Comment on the morphology of the erythrocytes.
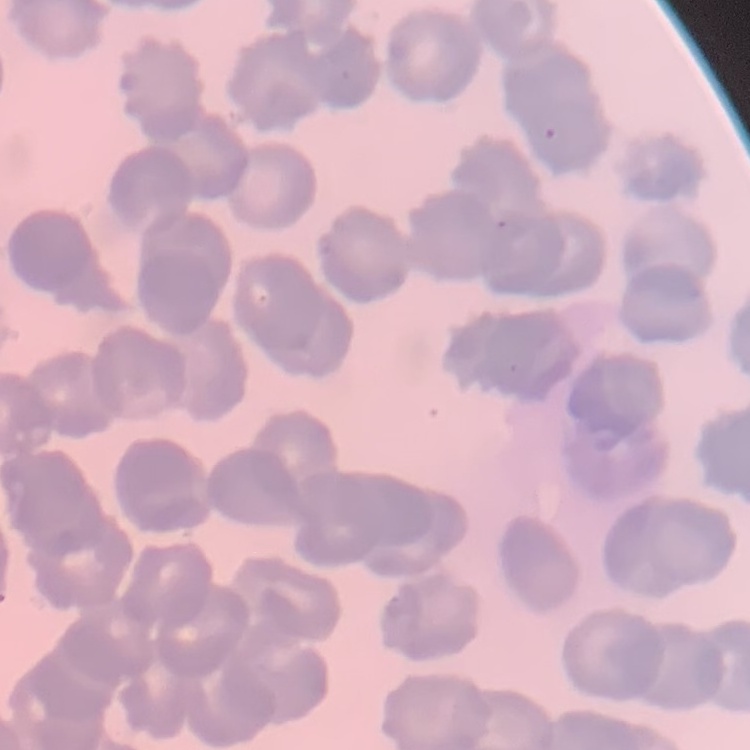
Rouleaux formation.

Summary:
  - Stain: Field's or Giemsa
  - Preparation: thin blood smear
  - Image type: square crop of a larger photomicrograph